Classify this cell by malaria status.
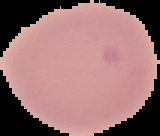
It is uninfected.

Summary:
  - Image type: segmented cell region on a black background
  - Image size: 160×136 pixels
  - Preparation: thin blood smear